Locate every Plasmodium parasite.
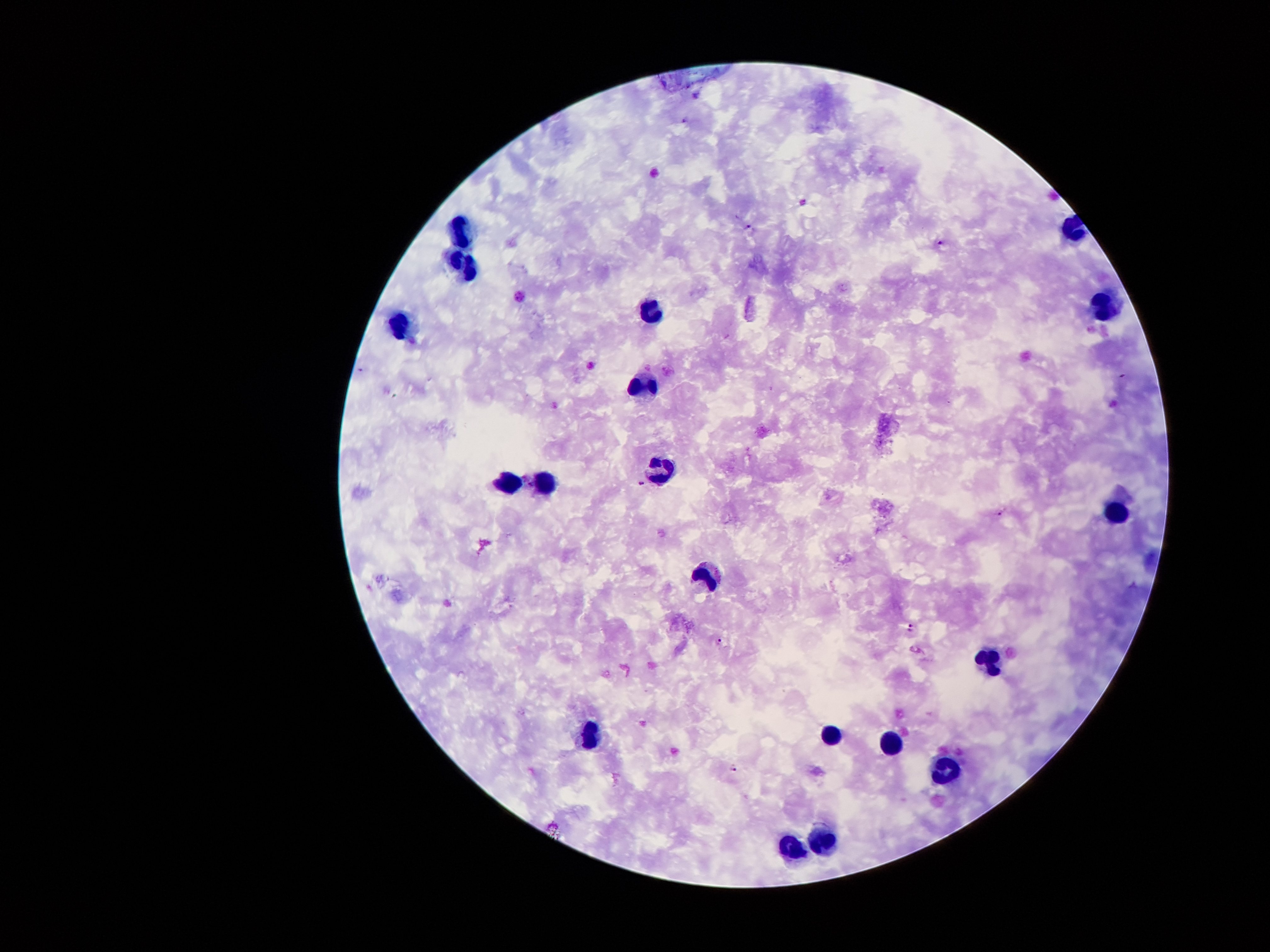
Approximate centers as {x, y} in pixels.
Plasmodium parasites: {750, 227}, {941, 243}, {644, 483}, {1001, 512}, {912, 630}, {722, 642}, {734, 767}.

Summary:
  - Leukocyte locations: {462, 230}, {465, 264}, {1104, 309}, {654, 311}, {396, 322}, {641, 387}, {668, 463}, {512, 484}, {550, 485}, {1115, 512}, {706, 572}, {989, 658}, {589, 731}, {829, 736}, {891, 744}, {947, 771}, {823, 837}, {794, 849}
  - Patient malaria status: infected with Plasmodium falciparum
  - Magnification: 100x
  - Field of view: one from this slide
  - Image size: 1270×952 pixels
  - Capture: smartphone camera through the microscope eyepiece
  - Preparation: thick blood film
  - Stain: Giemsa